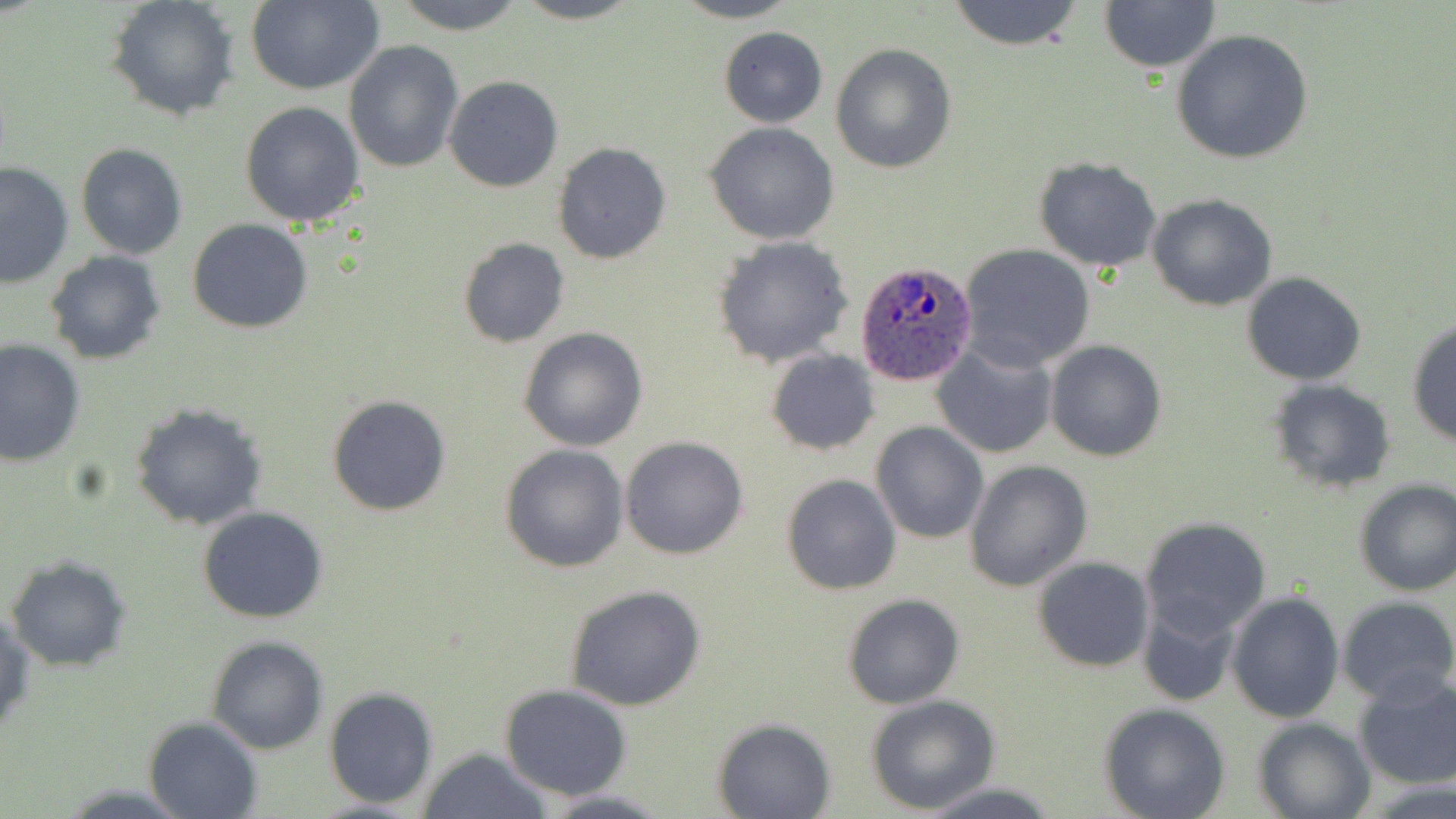
slide-level diagnosis = Plasmodium ovale
modality = light microscopy
image size = 1456×819 pixels
uninfected red blood cell locations = approximate bounding boxes as (x1,y1)-(x2,y2) corner pairs in pixels: (105,0)-(241,121), (390,0)-(530,34), (512,0)-(644,24), (672,0)-(802,24), (947,0)-(1082,50), (244,1)-(384,94), (1097,1)-(1221,73), (718,27)-(827,127), (1170,28)-(1314,164), (345,40)-(463,174), (831,43)-(958,175), (444,75)-(563,191), (239,101)-(366,229), (704,122)-(840,245), (552,142)-(670,264), (75,143)-(189,260), (1033,157)-(1163,272), (0,161)-(75,287), (1146,194)-(1277,310), (187,218)-(313,334), (713,235)-(854,367), (459,237)-(569,348), (959,243)-(1096,370), (44,252)-(165,365), (1241,272)-(1366,386), (1406,316)-(1455,447), (517,327)-(649,451), (0,339)-(84,466), (1045,340)-(1166,461), (931,342)-(1057,459), (765,349)-(880,456), (1267,380)-(1397,493), (326,393)-(451,516), (130,402)-(269,530), (871,420)-(988,544), (621,435)-(749,558), (500,444)-(629,572), (963,459)-(1093,591), (780,473)-(902,595), (1353,479)-(1455,596), (197,506)-(330,623), (1140,516)-(1272,636), (6,555)-(130,671), (1033,556)-(1153,671), (564,583)-(705,712), (1227,590)-(1344,722), (843,594)-(965,709), (1336,594)-(1456,706), (1136,596)-(1244,708), (1,609)-(35,740), (207,635)-(328,754), (1354,672)-(1456,791), (499,684)-(630,800), (323,687)-(438,810), (864,694)-(1002,813), (1099,703)-(1232,819), (145,716)-(263,818), (1253,716)-(1375,819), (712,717)-(835,817), (418,747)-(551,818), (920,781)-(1062,818), (535,789)-(673,819)
magnification = 1000x
preparation = thin blood smear
Plasmodium ovale-infected red blood cell locations = approximate bounding boxes as (x1,y1)-(x2,y2) corner pairs in pixels: (855,260)-(978,387)
stain = May-Grünwald-Giemsa
field of view = single